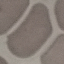
result = negative for malaria parasites
image type = automatically extracted cell patch, resized to 64 × 64 pixels
capture = smartphone camera at the microscope eyepiece
preparation = thin blood film
stain = Giemsa